Name the cell type shown.
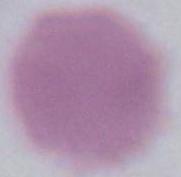

An erythrocyte.

Captured at 1000x magnification. Micrograph.